Identify the parasite.
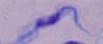
This is a trypanosome.

1000x magnification. Micrograph.